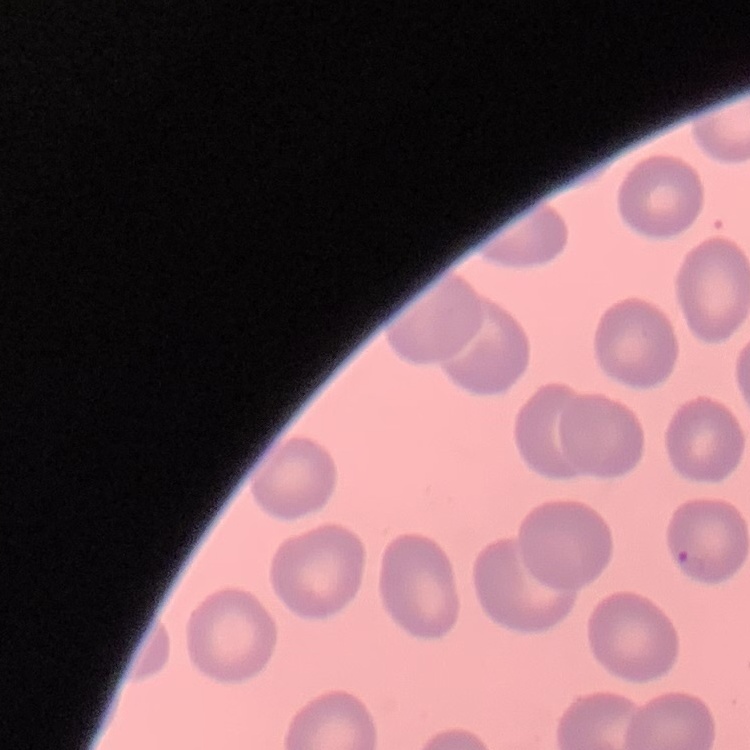
Summary:
  - Red blood cell morphology: no rouleaux formation
  - Stain: Field's or Giemsa
  - Preparation: thin blood smear
  - Image type: square crop of a larger photomicrograph